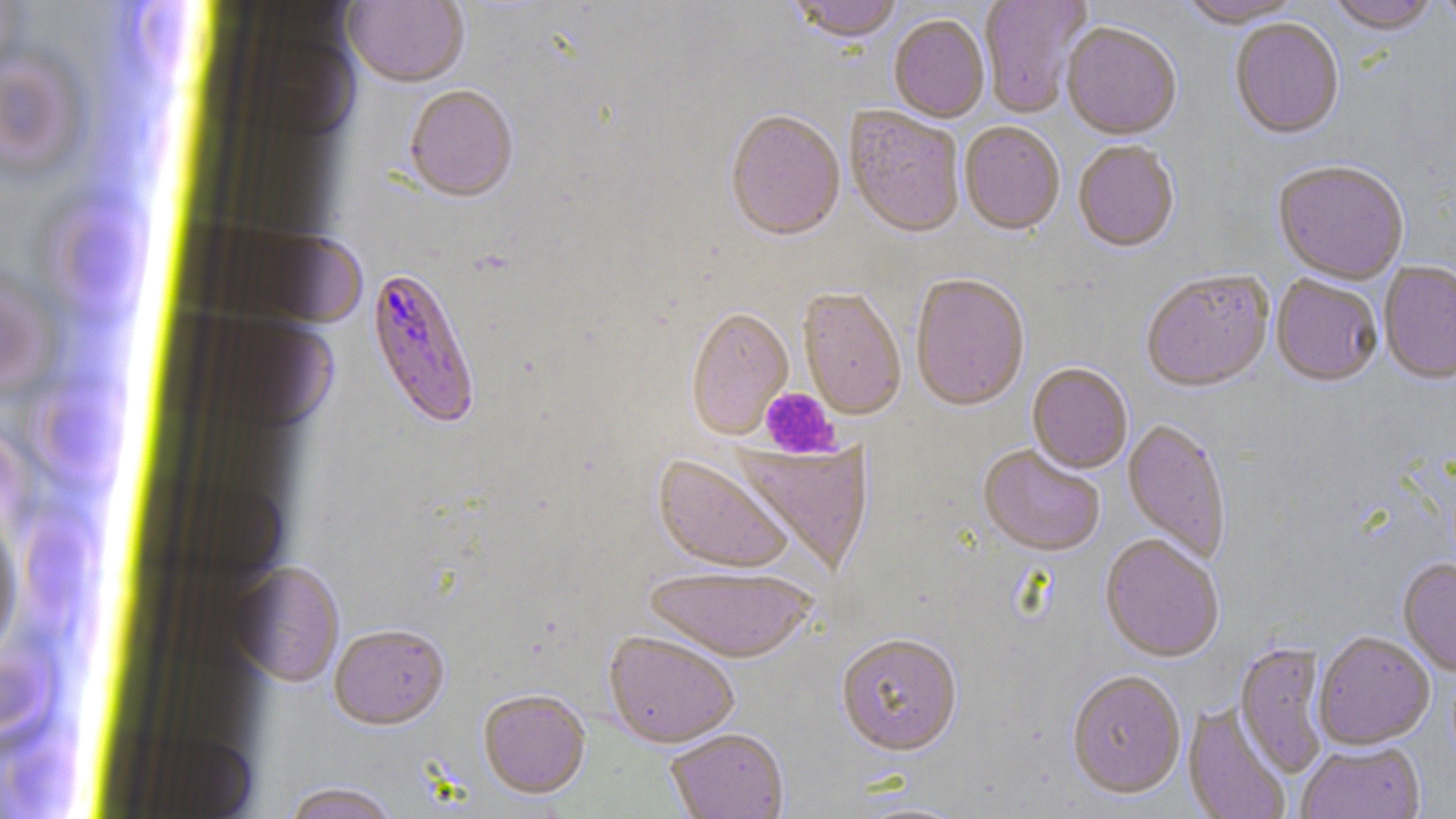
Plasmodium falciparum-infected red blood cell locations = approximate bounding boxes as [x1, y1, x2, y2] in pixels: [366, 265, 482, 431]
slide-level diagnosis = Plasmodium falciparum
magnification = 1000x
image size = 1456×819 pixels
platelet locations = approximate bounding boxes as [x1, y1, x2, y2] in pixels: [760, 388, 838, 459]
uninfected red blood cell locations = approximate bounding boxes as [x1, y1, x2, y2] in pixels: [0, 0, 31, 83], [787, 0, 904, 47], [979, 0, 1092, 118], [1178, 0, 1305, 30], [1326, 0, 1439, 37], [1437, 0, 1456, 33], [343, 1, 469, 90], [888, 17, 989, 125], [1229, 20, 1345, 142], [1062, 25, 1181, 142], [0, 46, 87, 184], [404, 87, 519, 205], [844, 108, 965, 240], [725, 112, 845, 244], [959, 123, 1065, 238], [1073, 143, 1179, 254], [1272, 163, 1409, 286], [1379, 262, 1456, 386], [1141, 271, 1274, 395], [911, 276, 1030, 412], [1271, 276, 1382, 389], [798, 290, 906, 421], [685, 309, 794, 442], [1027, 364, 1132, 475], [1123, 420, 1231, 563], [731, 439, 875, 576], [978, 446, 1104, 558], [653, 455, 794, 575], [0, 504, 23, 667], [1100, 536, 1225, 664], [1398, 559, 1456, 677], [231, 562, 344, 687], [645, 567, 818, 665], [329, 625, 450, 732], [602, 632, 740, 749], [1313, 634, 1435, 751], [836, 636, 963, 759], [1235, 643, 1329, 778], [1066, 671, 1186, 801], [478, 690, 591, 800], [1182, 702, 1291, 819], [665, 729, 790, 819], [1297, 742, 1426, 819], [280, 782, 402, 818]
preparation = thin blood smear
field of view = one of a larger specimen
modality = light microscopy
stain = May-Grünwald-Giemsa